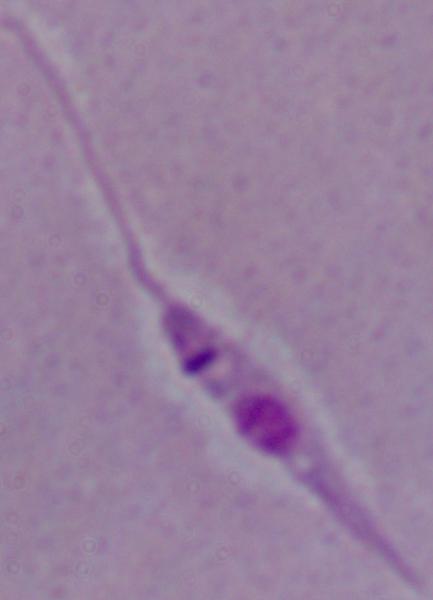
Photomicrograph. 1000x magnification. A Leishmania parasite is seen.